Assess this cell for malaria.
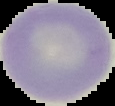
Uninfected.

image type = segmented cell region on a black background
preparation = thin blood film
image size = 115×106 pixels